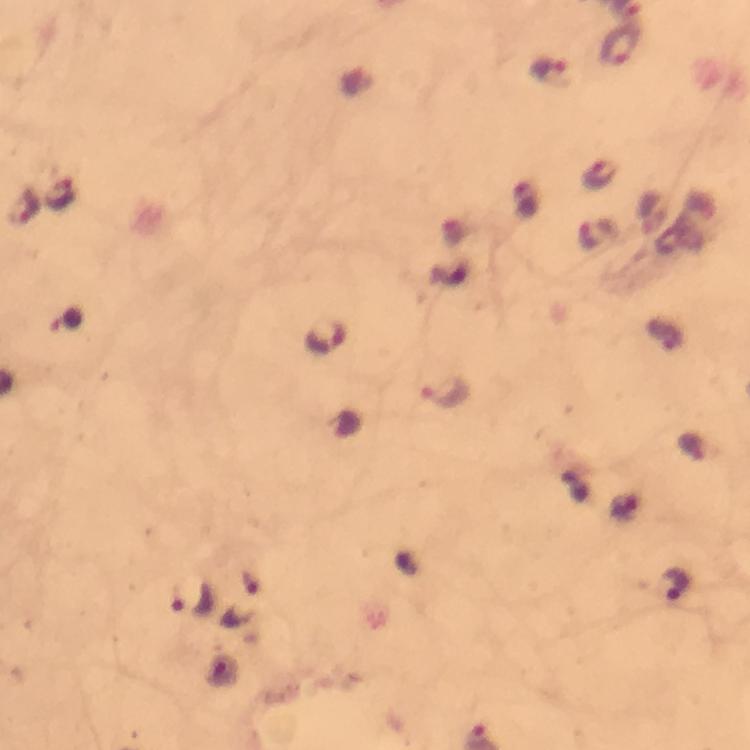
Approximate centers as [x, y] in pixels.
Summary:
  - Malaria parasite locations: [618, 47], [551, 71], [600, 176], [61, 196], [28, 208], [596, 234], [67, 322], [325, 337], [444, 393], [676, 583], [192, 600]
  - Preparation: thick blood smear
  - Stain: Giemsa
  - Context: from a diagnostic examination for malaria
  - Cropped from: a single field of view
  - Capture: smartphone camera through the microscope
  - Image size: 750×750 pixels
  - Immersion oil: used
  - Magnification: 100x